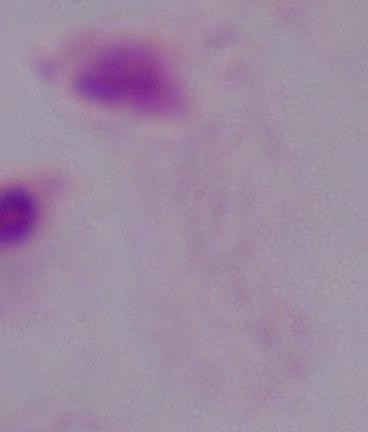

modality = photomicrograph
identification = trichomonad
magnification = 1000x